Locate and identify every blood parasite.
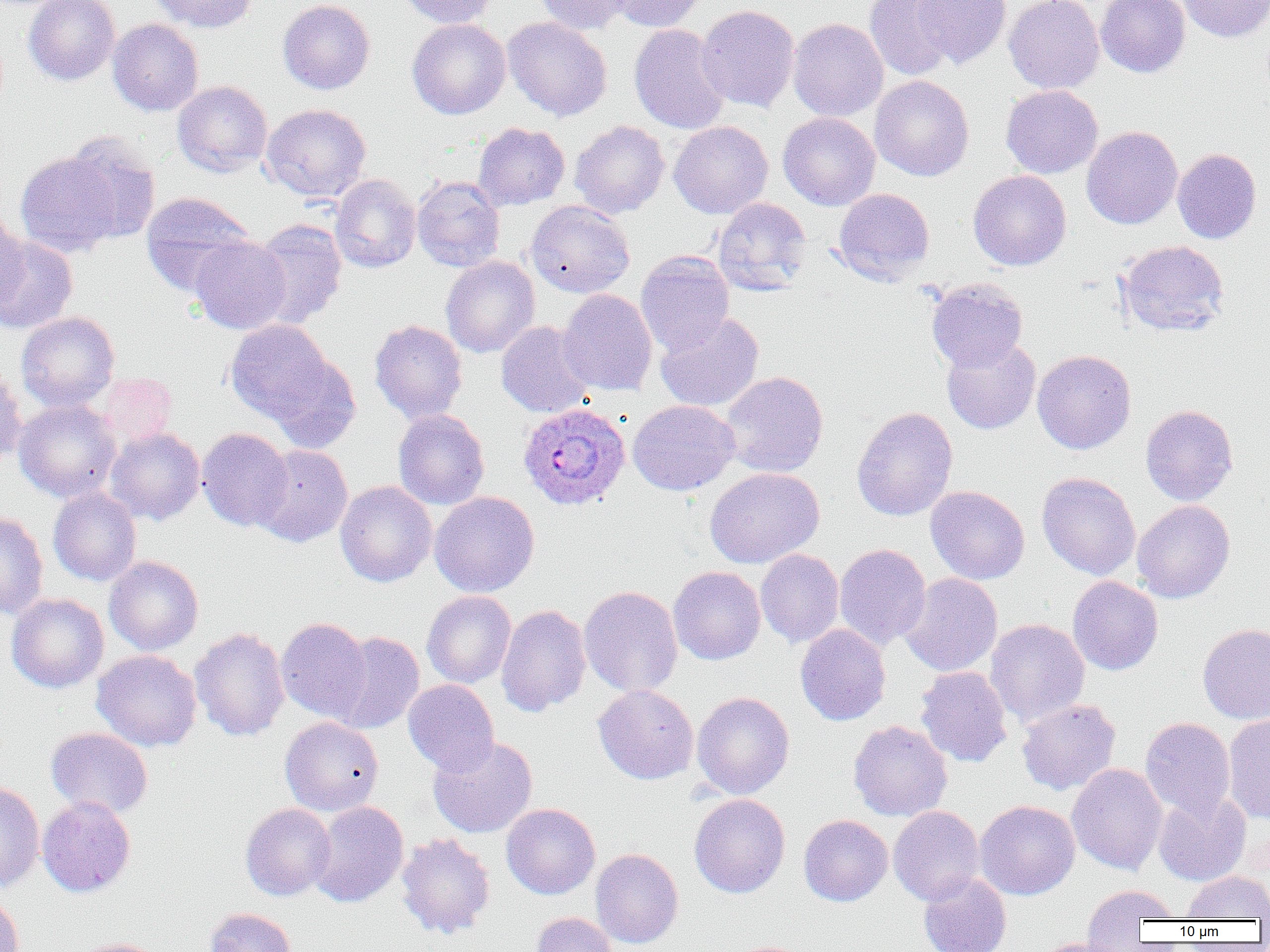
Approximate bounding boxes as (x1, y1, x2, y2) in pixels.
Plasmodium ovale-infected red blood cells: (518, 403, 630, 511).
No Plasmodium falciparum, Plasmodium malariae, Plasmodium vivax, Babesia divergens, or Trypanosoma brucei observed.

Summary:
  - Uninfected red blood cell locations: (23, 0, 120, 86), (149, 0, 259, 33), (277, 0, 375, 95), (400, 0, 501, 28), (534, 0, 632, 34), (608, 0, 705, 32), (864, 0, 960, 80), (912, 0, 1012, 69), (1004, 0, 1104, 94), (1095, 0, 1190, 78), (1178, 0, 1270, 43), (695, 4, 799, 113), (502, 17, 612, 121), (407, 18, 511, 119), (788, 18, 888, 122), (107, 19, 204, 116), (629, 24, 731, 135), (870, 75, 974, 181), (172, 80, 273, 177), (1000, 84, 1103, 178), (260, 103, 372, 202), (777, 112, 880, 210), (569, 120, 670, 218), (669, 121, 773, 218), (473, 122, 570, 210), (1081, 126, 1183, 229), (59, 134, 161, 246), (1172, 148, 1262, 244), (15, 150, 126, 257), (968, 170, 1071, 271), (330, 174, 421, 273), (412, 176, 505, 272), (832, 188, 935, 284), (140, 192, 256, 296), (712, 197, 812, 295), (526, 200, 635, 298), (0, 208, 28, 315), (250, 218, 347, 329), (0, 235, 78, 334), (190, 235, 292, 334), (1116, 240, 1230, 337), (635, 251, 735, 355), (441, 255, 540, 358), (926, 278, 1028, 371), (558, 289, 658, 396), (16, 311, 120, 411), (654, 311, 764, 412), (369, 319, 468, 424), (224, 320, 335, 425), (496, 321, 596, 418), (941, 336, 1041, 435), (1032, 349, 1136, 454), (263, 350, 362, 453), (0, 365, 27, 467), (92, 371, 178, 448), (718, 371, 828, 478), (13, 399, 122, 502), (628, 400, 740, 495), (1140, 404, 1238, 506), (851, 407, 958, 521), (392, 409, 489, 510), (197, 427, 294, 531), (105, 428, 205, 524), (252, 444, 353, 547), (704, 467, 824, 568), (1037, 472, 1141, 580), (336, 481, 437, 587), (926, 485, 1030, 585), (48, 487, 141, 586), (429, 491, 540, 598), (1132, 500, 1235, 603), (0, 511, 49, 621), (834, 544, 931, 650), (755, 549, 844, 648), (104, 556, 203, 655), (668, 566, 766, 665), (900, 573, 1003, 677), (1067, 576, 1164, 675), (579, 585, 683, 698), (421, 591, 517, 688), (6, 593, 109, 693), (495, 604, 592, 717), (276, 617, 372, 722), (985, 619, 1090, 727), (795, 623, 891, 726), (1197, 623, 1270, 724), (189, 627, 290, 742), (328, 631, 425, 734), (91, 650, 202, 752), (915, 666, 1013, 768), (403, 679, 499, 774), (593, 685, 699, 784), (691, 691, 795, 799), (1017, 698, 1121, 795), (1223, 714, 1270, 824), (280, 716, 384, 816), (1140, 717, 1236, 821), (848, 720, 952, 821), (45, 727, 154, 818), (427, 735, 538, 838), (1067, 763, 1168, 875), (0, 781, 45, 893), (1153, 792, 1251, 886), (689, 793, 790, 898), (37, 797, 136, 897), (308, 800, 409, 908), (975, 800, 1080, 900), (240, 803, 336, 901), (501, 803, 601, 899), (888, 806, 985, 905), (798, 814, 893, 906), (397, 833, 495, 939), (590, 848, 684, 949), (1182, 871, 1270, 920), (918, 872, 1012, 952), (1081, 884, 1180, 947), (0, 892, 25, 952), (203, 907, 297, 952), (531, 912, 618, 952), (69, 937, 170, 952), (1033, 938, 1132, 952)
  - Slide-level diagnosis: Plasmodium ovale
  - Magnification: 1000x
  - Field of view: single
  - Image size: 1270×952 pixels
  - Preparation: thin blood smear
  - Modality: optical microscopy